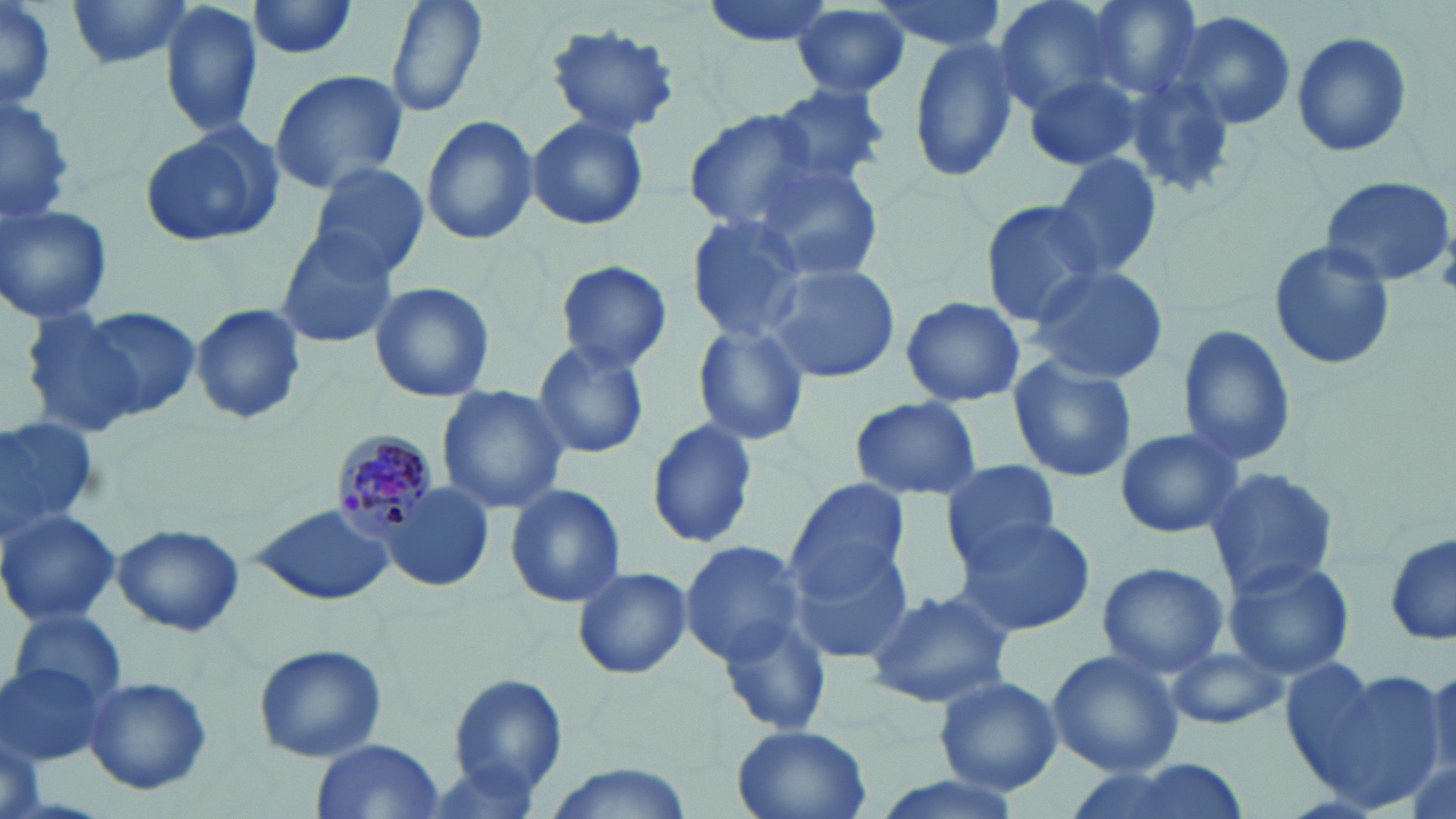

slide_level_diagnosis: Plasmodium malariae
preparation: thin blood film
magnification: 1000x
uninfected_red_blood_cell_locations: 'approximate bounding boxes as (x1, y1, x2, y2) in pixels: (66, 0, 196, 70), (159, 0, 264, 138), (384, 0, 488, 121), (700, 0, 844, 48), (865, 0, 1008, 52), (991, 0, 1129, 116), (1085, 0, 1203, 100), (246, 1, 363, 60), (0, 4, 58, 110), (788, 5, 911, 99), (1169, 10, 1297, 131), (544, 23, 682, 137), (1290, 28, 1414, 159), (907, 36, 1024, 183), (1022, 65, 1145, 171), (268, 69, 408, 196), (1121, 72, 1245, 202), (764, 83, 892, 194), (1, 92, 76, 226), (685, 109, 821, 234), (422, 114, 538, 248), (525, 114, 649, 233), (138, 125, 282, 248), (1050, 153, 1164, 281), (307, 161, 429, 280), (751, 161, 885, 284), (1318, 174, 1455, 291), (979, 199, 1104, 324), (0, 203, 113, 323), (683, 214, 813, 343), (274, 228, 403, 350), (1268, 240, 1394, 373), (555, 260, 673, 373), (759, 261, 899, 384), (1022, 265, 1169, 384), (368, 281, 495, 404), (899, 294, 1026, 408), (190, 304, 310, 425), (77, 307, 201, 420), (20, 309, 151, 439), (1176, 322, 1297, 469), (691, 323, 812, 449), (530, 338, 652, 461), (1008, 354, 1137, 484), (436, 386, 570, 515), (848, 396, 983, 502), (0, 415, 101, 534), (647, 419, 755, 549), (1115, 428, 1244, 538), (941, 460, 1062, 566), (1203, 467, 1340, 597), (787, 479, 910, 599), (504, 484, 626, 609), (382, 487, 495, 592), (249, 504, 395, 605), (0, 507, 120, 629), (948, 514, 1097, 637), (113, 523, 244, 637), (1385, 534, 1455, 648), (677, 539, 810, 665), (785, 539, 913, 663), (1221, 556, 1356, 680), (1097, 559, 1230, 678), (572, 566, 692, 679), (863, 586, 1015, 710), (10, 607, 127, 711), (715, 608, 834, 739), (253, 642, 388, 763), (1165, 643, 1284, 730), (1046, 649, 1184, 779), (0, 659, 106, 768), (1281, 659, 1436, 804), (1421, 661, 1456, 781), (448, 673, 569, 797), (934, 676, 1063, 796), (81, 678, 213, 795), (731, 725, 873, 818), (0, 733, 44, 819), (311, 739, 446, 817), (1070, 758, 1253, 819), (861, 775, 1028, 819)'
image_size: 1456×819 pixels
field_of_view: single
plasmodium_malariae_infected_red_blood_cell_locations: 'approximate bounding boxes as (x1, y1, x2, y2) in pixels: (329, 427, 447, 538)'
modality: light microscopy
stain: May-Grünwald-Giemsa